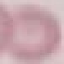

malaria_status: uninfected
stain: Giemsa
capture: smartphone through the microscope eyepiece
preparation: thin smear
image_type: cell patch, automatically extracted from a larger field of view and resized to 64 × 64 pixels